Locate every Plasmodium parasite.
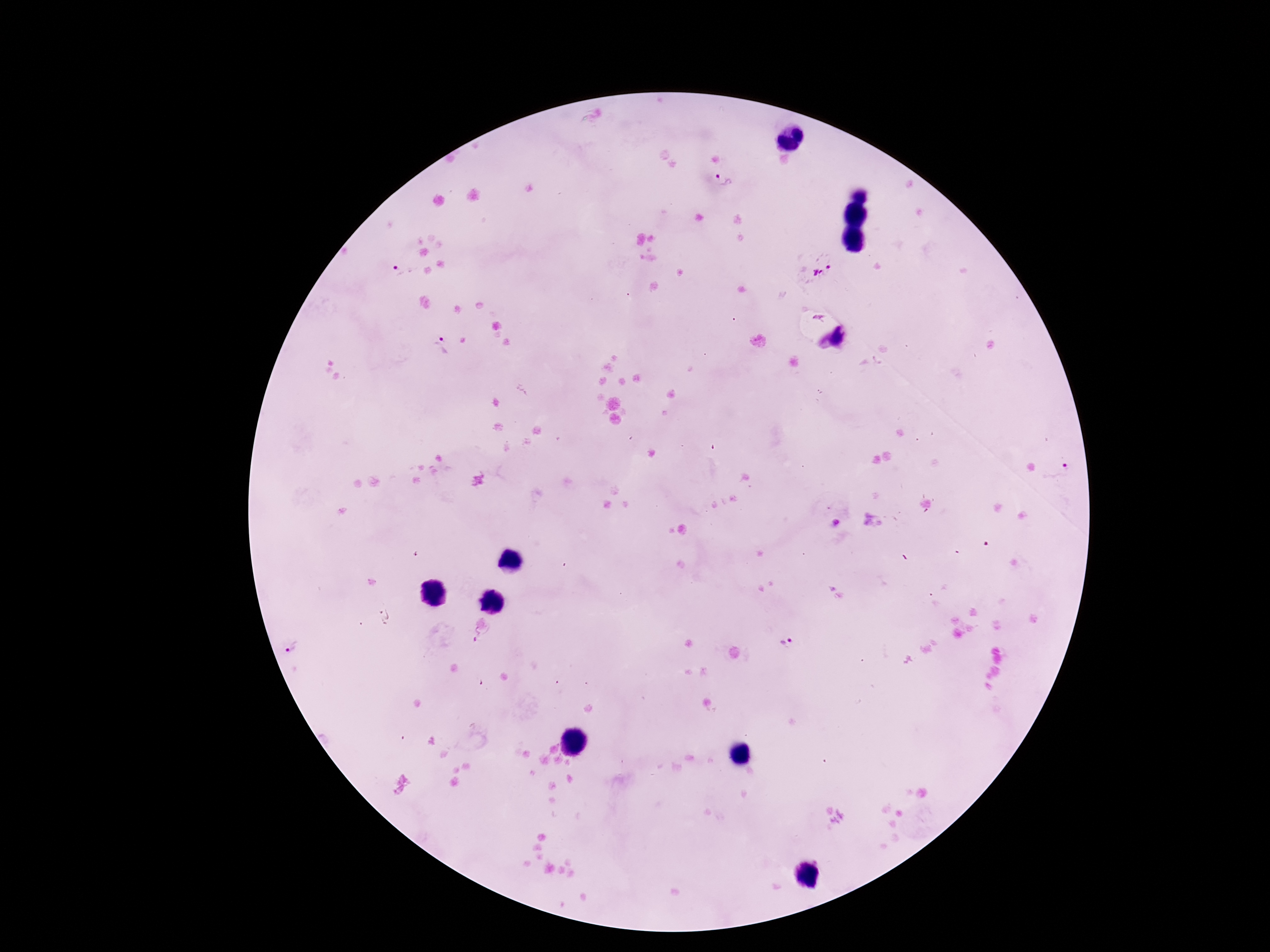

Approximate object centers, in pixels from the top-left corner.
Plasmodium parasites: (x=724, y=181), (x=814, y=268), (x=404, y=271), (x=821, y=318), (x=842, y=337), (x=440, y=344), (x=1056, y=474), (x=474, y=638), (x=789, y=643), (x=292, y=646).

Patient malaria status: positive. Giemsa stain. Thick blood smear. Image is 1270×952 pixels. One field from this slide. Smartphone photograph taken through the microscope eyepiece. 100x magnification.